Describe the morphology of the erythrocytes.
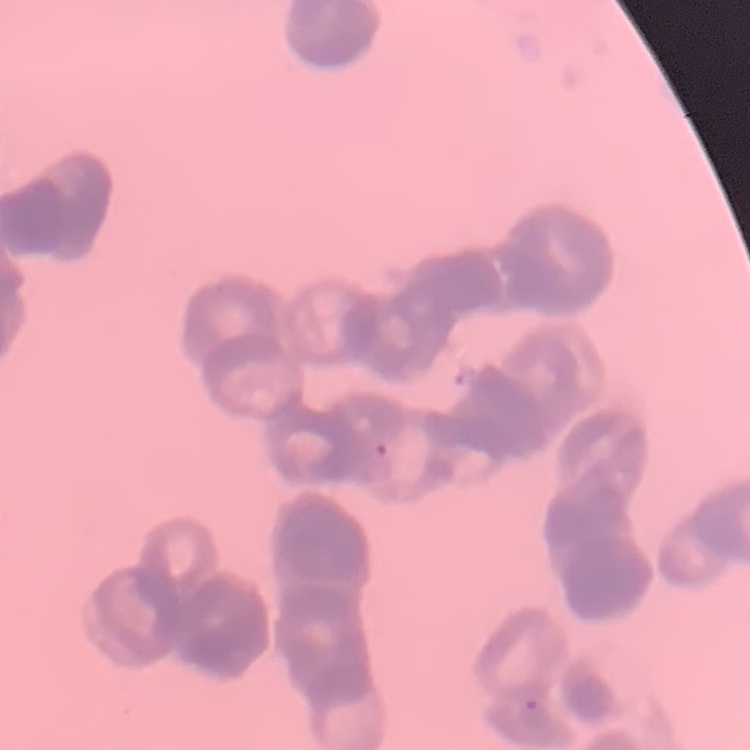

Rouleaux formation.

Summary:
  - Image type: square crop of a larger photomicrograph
  - Stain: Field's or Giemsa
  - Preparation: thin blood film